Give the position of every leukocyte visible.
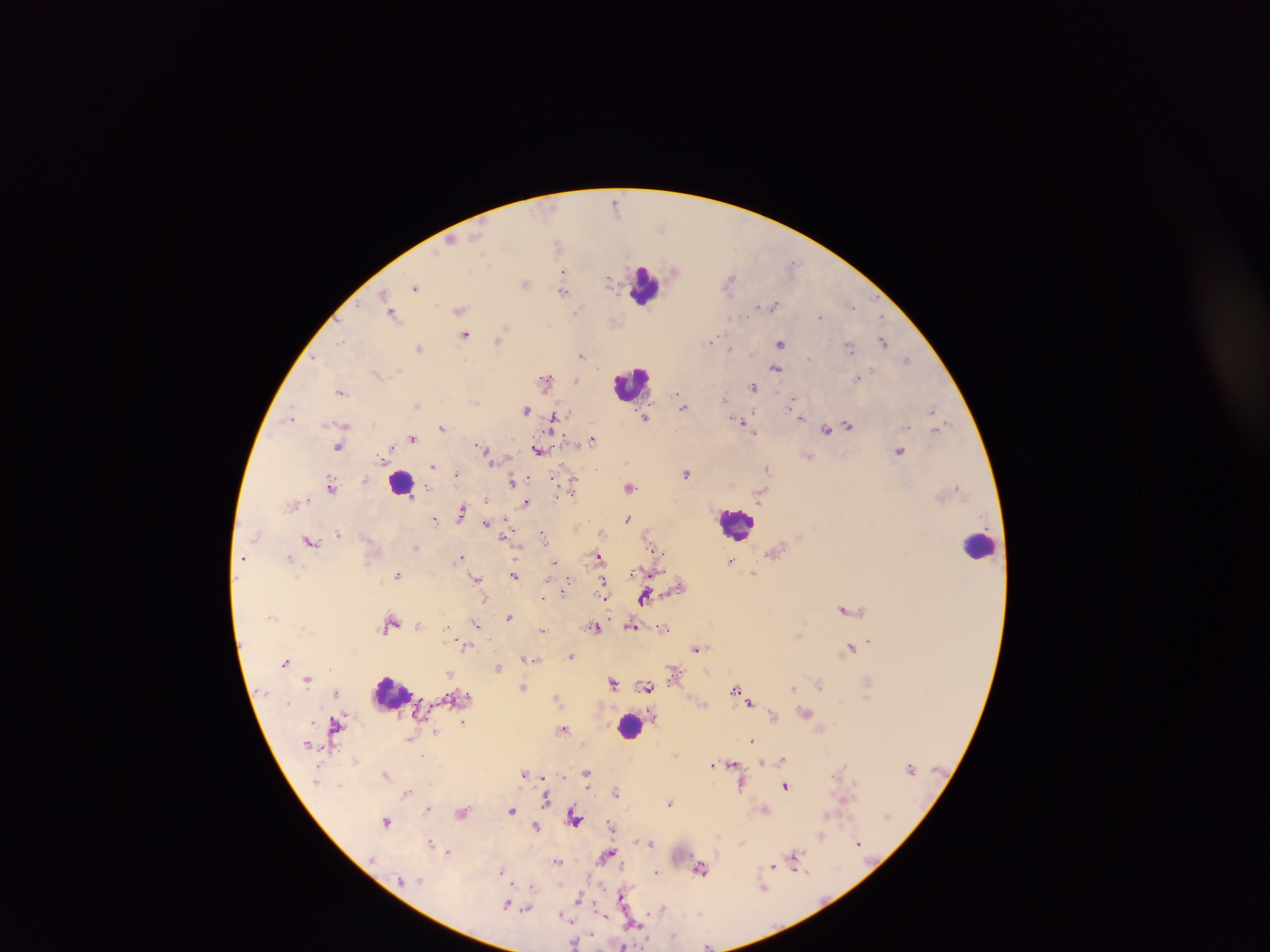
Approximate centers as [x, y] in pixels.
Leukocytes: [645, 286], [630, 383], [401, 482], [736, 524], [980, 546], [391, 693], [630, 724].

plasmodium_parasite_locations: 'approximate centers as [x, y] in pixels: [616, 203], [662, 226], [451, 241], [556, 244], [793, 263], [674, 270], [563, 272], [610, 280], [729, 281], [525, 283], [416, 287], [564, 290], [383, 294], [773, 305], [851, 306], [460, 310], [577, 310], [393, 314], [819, 317], [506, 328], [466, 335], [500, 338], [714, 340], [340, 341], [883, 341], [780, 344], [420, 347], [849, 347], [730, 348], [581, 355], [809, 358], [316, 359], [907, 359], [776, 369], [872, 370], [376, 373], [857, 378], [546, 379], [577, 380], [754, 386], [341, 391], [679, 395], [725, 398], [793, 402], [417, 405], [682, 405], [526, 409], [932, 410], [292, 415], [645, 416], [554, 417], [800, 417], [742, 423], [345, 425], [849, 425], [442, 427], [939, 428], [826, 430], [753, 431], [413, 438], [593, 440], [339, 446], [481, 446], [537, 450], [900, 450], [382, 457], [433, 466], [767, 469], [687, 473], [365, 479], [555, 480], [512, 481], [331, 485], [960, 486], [630, 487], [573, 489], [486, 498], [526, 503], [462, 513], [435, 519], [627, 519], [486, 522], [542, 533], [339, 534], [505, 537], [309, 540], [657, 550], [289, 556], [598, 556], [244, 557], [460, 557], [731, 561], [555, 562], [754, 574], [397, 575], [514, 575], [476, 579], [603, 583], [564, 589], [604, 594], [645, 596], [606, 598], [843, 608], [509, 616], [392, 622], [477, 625], [631, 625], [596, 627], [662, 628], [544, 630], [799, 635], [869, 640], [461, 645], [696, 648], [850, 648], [571, 656], [526, 658], [531, 659], [285, 662], [499, 667], [449, 674], [308, 679], [613, 683], [819, 684], [523, 687], [648, 687], [735, 688], [793, 688], [335, 693], [751, 703], [806, 712], [772, 715], [463, 723], [336, 724], [563, 728], [436, 732], [410, 739], [752, 739], [783, 758], [762, 763], [713, 764], [733, 765], [525, 773], [587, 773], [386, 775], [741, 785], [785, 786], [406, 793], [616, 793], [546, 799], [669, 804], [427, 809], [765, 809], [511, 810], [463, 813], [828, 814], [574, 818], [386, 821], [611, 825], [536, 827], [821, 837], [858, 841], [431, 842], [652, 843], [449, 852], [606, 854], [796, 854], [557, 862], [622, 865], [773, 866], [702, 869], [502, 871], [656, 871], [802, 871], [532, 888], [763, 888], [623, 896], [579, 898], [507, 905], [527, 909], [663, 910], [599, 913], [563, 916], [635, 925], [674, 936], [575, 942], [624, 946], [707, 946]'
country: Ghana
image_size: 1270×952 pixels
preparation: thick blood smear
capture: mobile-phone photograph through a microscope
field_of_view: single